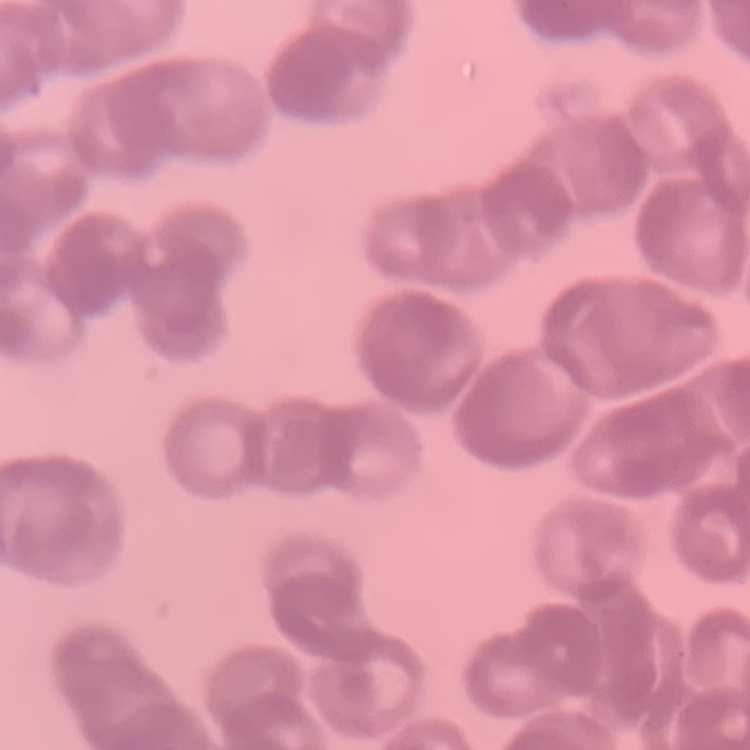
{
  "red_blood_cell_morphology": "rouleaux formation",
  "preparation": "thin peripheral smear",
  "stain": "Field's or Giemsa",
  "image_type": "one tile cut from a larger photomicrograph"
}